Name the parasite shown.
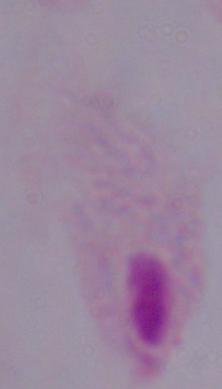

A trichomonad.

modality = micrograph
magnification = 1000x